Identify the blood parasite species.
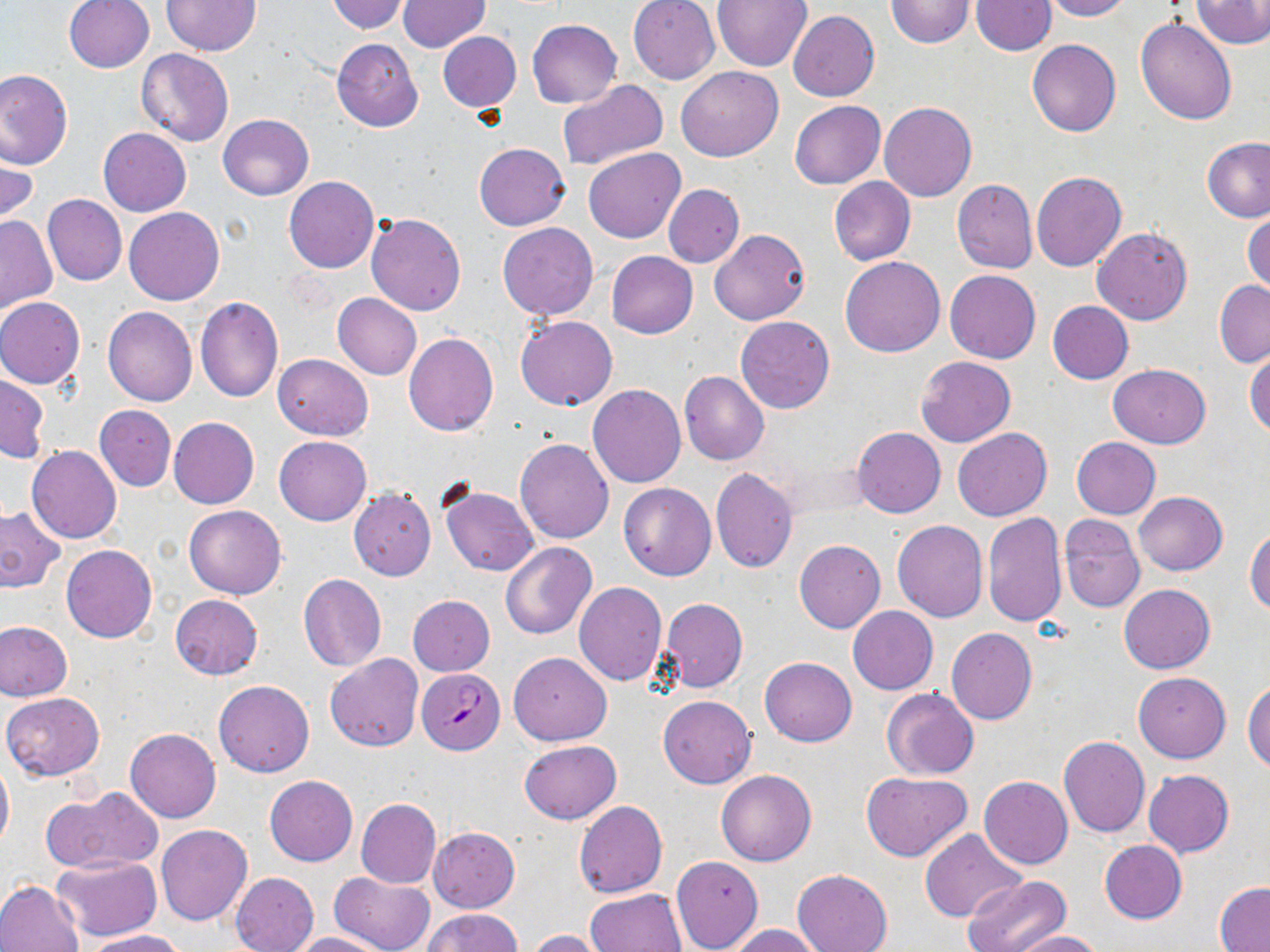

Plasmodium falciparum.

stain: May-Grünwald-Giemsa
modality: light microscopy
image_size: 1270×952 pixels
preparation: thin blood smear
field_of_view: single
uninfected_red_blood_cell_locations: 'approximate bounding boxes as [x1, y1, x2, y2] in pixels: [62, 0, 154, 74], [161, 0, 260, 55], [326, 0, 411, 34], [628, 0, 720, 84], [886, 0, 975, 48], [1040, 0, 1132, 21], [1192, 0, 1270, 49], [398, 1, 489, 51], [711, 1, 812, 72], [970, 1, 1055, 56], [789, 10, 879, 101], [1136, 17, 1237, 125], [528, 19, 622, 106], [437, 31, 520, 112], [331, 38, 423, 131], [1027, 40, 1120, 137], [136, 48, 234, 148], [675, 65, 784, 162], [0, 69, 72, 170], [557, 80, 668, 169], [789, 101, 885, 188], [879, 101, 977, 202], [218, 114, 313, 200], [99, 128, 191, 216], [1202, 137, 1270, 222], [474, 143, 571, 230], [583, 147, 685, 243], [1, 148, 37, 227], [1032, 171, 1127, 272], [284, 176, 378, 273], [829, 177, 916, 265], [952, 179, 1038, 274], [664, 184, 744, 268], [42, 194, 126, 287], [124, 207, 224, 305], [1244, 211, 1270, 296], [366, 212, 466, 316], [0, 214, 57, 314], [497, 222, 598, 320], [1093, 227, 1192, 325], [710, 229, 809, 326], [606, 251, 698, 339], [840, 256, 946, 358], [944, 269, 1040, 363], [1215, 280, 1270, 369], [332, 293, 422, 380], [195, 295, 283, 402], [0, 298, 85, 388], [1047, 301, 1133, 384], [102, 305, 198, 406], [515, 315, 618, 410], [735, 315, 835, 414], [403, 334, 498, 437], [1245, 347, 1270, 438], [273, 353, 372, 440], [916, 356, 1016, 446], [1107, 364, 1212, 448], [679, 371, 769, 465], [0, 374, 48, 461], [588, 384, 687, 488], [95, 405, 176, 491], [169, 417, 259, 510], [853, 427, 946, 518], [952, 428, 1053, 522], [275, 436, 370, 526], [515, 437, 614, 543], [1071, 438, 1160, 520], [26, 446, 122, 544], [710, 468, 798, 572], [618, 483, 716, 581], [439, 484, 540, 577], [349, 489, 435, 580], [1134, 491, 1227, 576], [183, 504, 287, 599], [0, 506, 65, 592], [983, 511, 1066, 627], [1058, 514, 1145, 613], [892, 520, 988, 622], [1247, 526, 1270, 617], [794, 539, 885, 633], [501, 543, 596, 640], [61, 544, 157, 643], [298, 575, 386, 672], [574, 582, 667, 685], [1119, 583, 1215, 673], [171, 595, 263, 679], [407, 595, 495, 675], [659, 598, 747, 693], [848, 607, 938, 694], [0, 620, 73, 701], [946, 627, 1037, 724], [508, 652, 611, 745], [326, 654, 424, 753], [760, 656, 857, 747], [1133, 673, 1230, 762], [1244, 678, 1270, 773], [213, 679, 314, 776], [881, 689, 979, 780], [2, 691, 105, 781], [657, 695, 756, 788], [124, 727, 221, 822], [1058, 735, 1150, 837], [518, 740, 621, 824], [0, 757, 13, 854], [1144, 769, 1235, 857], [860, 770, 972, 861], [716, 771, 816, 866], [265, 775, 358, 867], [979, 775, 1072, 869], [43, 785, 164, 874], [356, 798, 441, 888], [573, 801, 668, 898], [156, 825, 252, 926], [429, 827, 520, 911], [919, 829, 1028, 924], [1099, 840, 1187, 924], [51, 855, 159, 942], [670, 856, 763, 951], [792, 869, 893, 952], [329, 871, 434, 952], [231, 872, 318, 952], [963, 876, 1070, 952], [0, 880, 86, 952], [1215, 884, 1270, 951], [583, 888, 686, 951], [425, 908, 522, 952], [726, 924, 823, 952], [81, 928, 188, 951], [527, 929, 610, 951], [1009, 929, 1103, 951], [290, 932, 388, 952]'
plasmodium_falciparum_infected_red_blood_cell_locations: 'approximate bounding boxes as [x1, y1, x2, y2] in pixels: [417, 668, 504, 754]'
magnification: 1000x